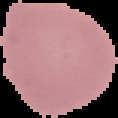

preparation = thin blood smear
image type = segmented cell region on a black background
malaria status = uninfected
image size = 118×118 pixels